Locate every uninfected red blood cell.
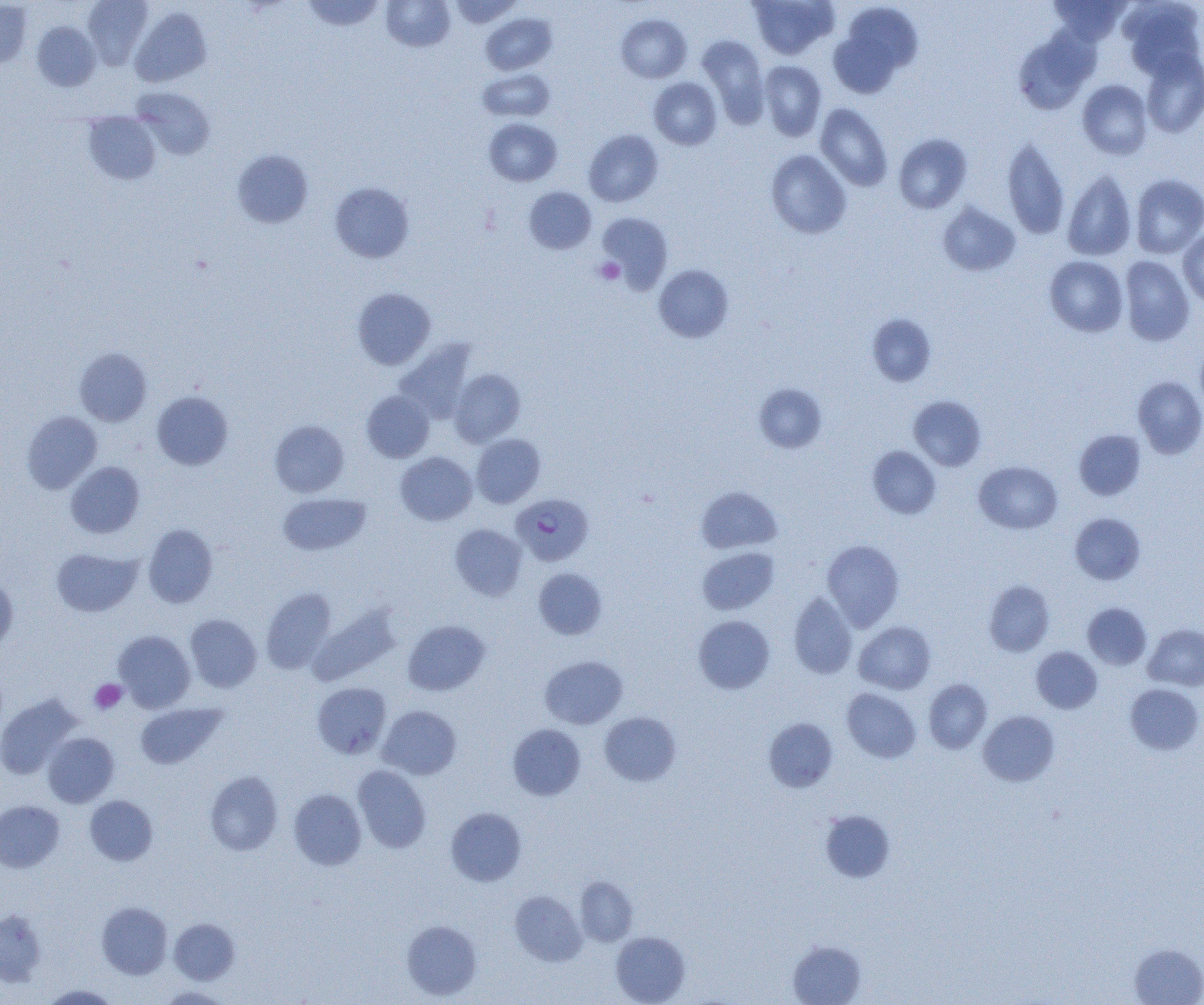

Approximate bounding boxes as named x1/y1/x2/y2 corners in pixels.
Uninfected red blood cells: (x1=83, y1=0, x2=152, y2=69), (x1=301, y1=0, x2=385, y2=31), (x1=381, y1=0, x2=455, y2=52), (x1=448, y1=0, x2=522, y2=27), (x1=749, y1=0, x2=838, y2=60), (x1=1049, y1=0, x2=1130, y2=45), (x1=0, y1=1, x2=33, y2=68), (x1=1119, y1=1, x2=1204, y2=79), (x1=832, y1=3, x2=922, y2=94), (x1=130, y1=7, x2=212, y2=87), (x1=481, y1=13, x2=557, y2=75), (x1=616, y1=14, x2=691, y2=83), (x1=32, y1=21, x2=100, y2=91), (x1=1013, y1=28, x2=1099, y2=114), (x1=697, y1=34, x2=769, y2=127), (x1=1140, y1=50, x2=1204, y2=138), (x1=759, y1=61, x2=826, y2=141), (x1=478, y1=68, x2=555, y2=122), (x1=649, y1=77, x2=722, y2=150), (x1=1077, y1=80, x2=1152, y2=159), (x1=132, y1=87, x2=215, y2=160), (x1=815, y1=103, x2=893, y2=191), (x1=83, y1=112, x2=161, y2=185), (x1=484, y1=118, x2=562, y2=186), (x1=584, y1=130, x2=663, y2=207), (x1=893, y1=134, x2=972, y2=214), (x1=1002, y1=137, x2=1070, y2=239), (x1=232, y1=150, x2=313, y2=228), (x1=766, y1=150, x2=851, y2=238), (x1=1062, y1=169, x2=1136, y2=261), (x1=1130, y1=174, x2=1204, y2=258), (x1=330, y1=182, x2=414, y2=263), (x1=524, y1=186, x2=596, y2=254), (x1=937, y1=202, x2=1020, y2=276), (x1=597, y1=213, x2=673, y2=291), (x1=1178, y1=228, x2=1204, y2=307), (x1=1045, y1=256, x2=1128, y2=337), (x1=1119, y1=256, x2=1195, y2=346), (x1=654, y1=264, x2=733, y2=343), (x1=352, y1=287, x2=435, y2=369), (x1=867, y1=314, x2=936, y2=386), (x1=1195, y1=338, x2=1204, y2=417), (x1=394, y1=339, x2=476, y2=423), (x1=74, y1=347, x2=152, y2=426), (x1=449, y1=369, x2=525, y2=447), (x1=1133, y1=375, x2=1204, y2=459), (x1=754, y1=383, x2=827, y2=453), (x1=152, y1=391, x2=233, y2=470), (x1=362, y1=391, x2=434, y2=462), (x1=908, y1=395, x2=986, y2=471), (x1=23, y1=411, x2=102, y2=493), (x1=270, y1=420, x2=349, y2=497), (x1=1074, y1=429, x2=1146, y2=500), (x1=472, y1=434, x2=545, y2=508), (x1=868, y1=445, x2=941, y2=519), (x1=395, y1=452, x2=477, y2=526), (x1=66, y1=461, x2=144, y2=538), (x1=974, y1=461, x2=1062, y2=534), (x1=696, y1=486, x2=782, y2=554), (x1=278, y1=492, x2=371, y2=556), (x1=1069, y1=513, x2=1145, y2=584), (x1=142, y1=524, x2=217, y2=608), (x1=450, y1=524, x2=527, y2=601), (x1=822, y1=539, x2=904, y2=631), (x1=697, y1=547, x2=779, y2=615), (x1=51, y1=548, x2=142, y2=617), (x1=533, y1=568, x2=607, y2=640), (x1=0, y1=577, x2=18, y2=654), (x1=984, y1=580, x2=1054, y2=656), (x1=260, y1=588, x2=337, y2=674), (x1=789, y1=592, x2=856, y2=678), (x1=1082, y1=602, x2=1151, y2=669), (x1=309, y1=604, x2=401, y2=686), (x1=185, y1=614, x2=262, y2=693), (x1=693, y1=615, x2=774, y2=694), (x1=403, y1=620, x2=489, y2=695), (x1=854, y1=621, x2=936, y2=694), (x1=1144, y1=624, x2=1204, y2=691), (x1=114, y1=630, x2=195, y2=713), (x1=1031, y1=646, x2=1102, y2=713), (x1=540, y1=655, x2=628, y2=729), (x1=924, y1=679, x2=992, y2=753), (x1=312, y1=682, x2=391, y2=758), (x1=1125, y1=683, x2=1203, y2=754), (x1=841, y1=688, x2=921, y2=763), (x1=0, y1=694, x2=81, y2=779), (x1=135, y1=702, x2=226, y2=769), (x1=378, y1=705, x2=461, y2=779), (x1=978, y1=710, x2=1059, y2=785), (x1=599, y1=711, x2=681, y2=786), (x1=763, y1=717, x2=838, y2=792), (x1=507, y1=723, x2=585, y2=800), (x1=42, y1=732, x2=119, y2=807), (x1=352, y1=766, x2=431, y2=853), (x1=205, y1=771, x2=282, y2=855), (x1=289, y1=788, x2=366, y2=870), (x1=85, y1=795, x2=157, y2=865), (x1=0, y1=800, x2=64, y2=872), (x1=446, y1=807, x2=527, y2=886), (x1=819, y1=809, x2=895, y2=883), (x1=575, y1=876, x2=638, y2=946), (x1=510, y1=890, x2=586, y2=966), (x1=96, y1=902, x2=172, y2=979), (x1=0, y1=910, x2=46, y2=987), (x1=170, y1=918, x2=239, y2=984), (x1=401, y1=920, x2=482, y2=1000), (x1=611, y1=931, x2=690, y2=1004), (x1=787, y1=939, x2=866, y2=1005), (x1=1129, y1=943, x2=1204, y2=1005), (x1=40, y1=984, x2=120, y2=1004), (x1=156, y1=986, x2=233, y2=1004).

Plasmodium falciparum-infected red blood cell locations: (x1=510, y1=493, x2=594, y2=566). Platelet locations: (x1=595, y1=257, x2=624, y2=285), (x1=90, y1=679, x2=127, y2=714). Slide-level diagnosis: Plasmodium falciparum. Single field of view. Thin blood film. Captured at 1000x magnification. Light microscopy. Image is 1204×1005 pixels.